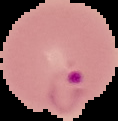
image type = segmented cell region on a black background
preparation = thin blood smear
malaria status = parasitized
image size = 118×121 pixels